Identify the preparation type.
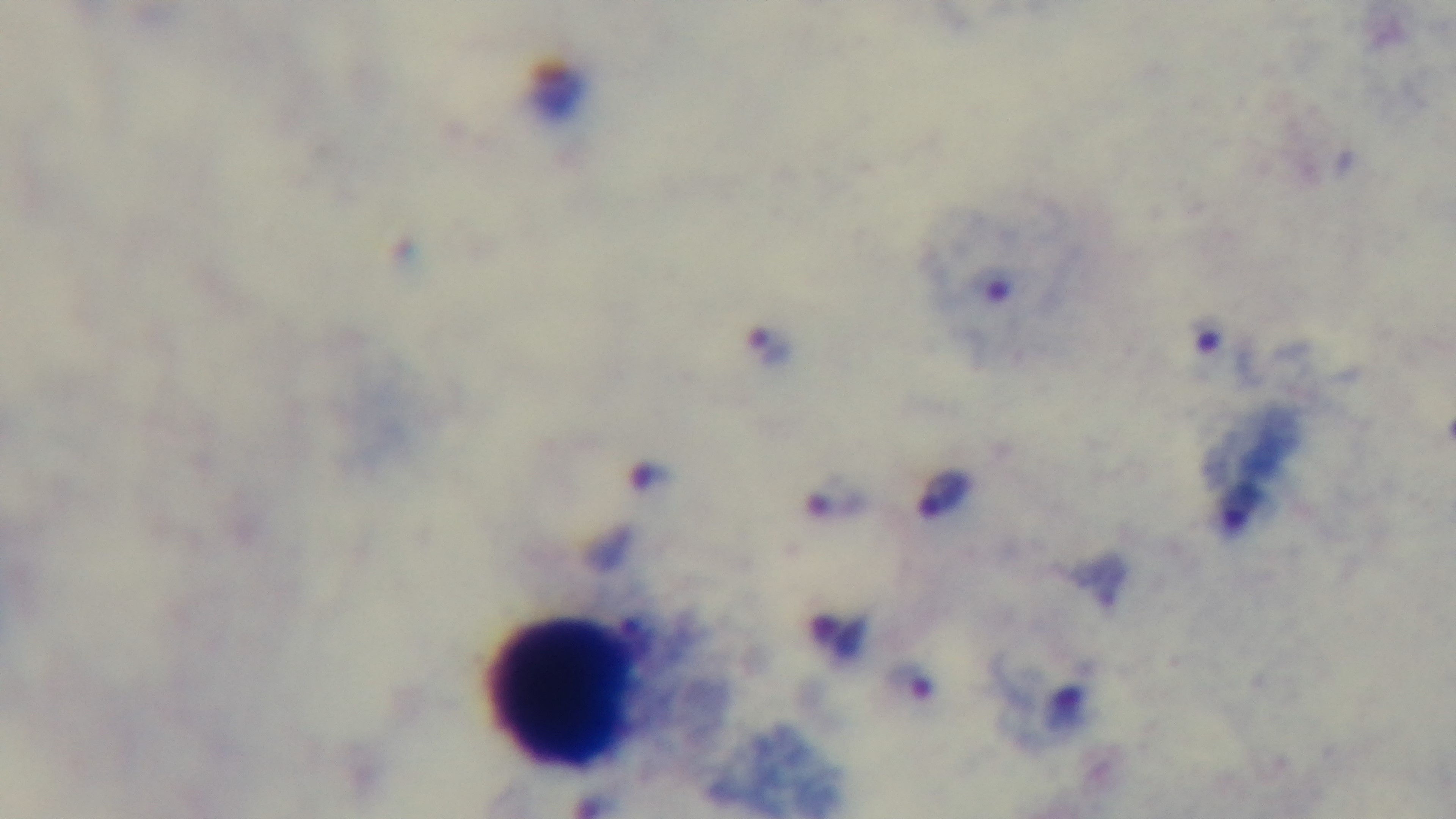
Thick.

One field from the slide. Giemsa-stained. Malaria status: positive. Oil-immersion objective, 100x. Photomicrograph. Mounted 4K digital camera.